Give the position of every leukocyte visible.
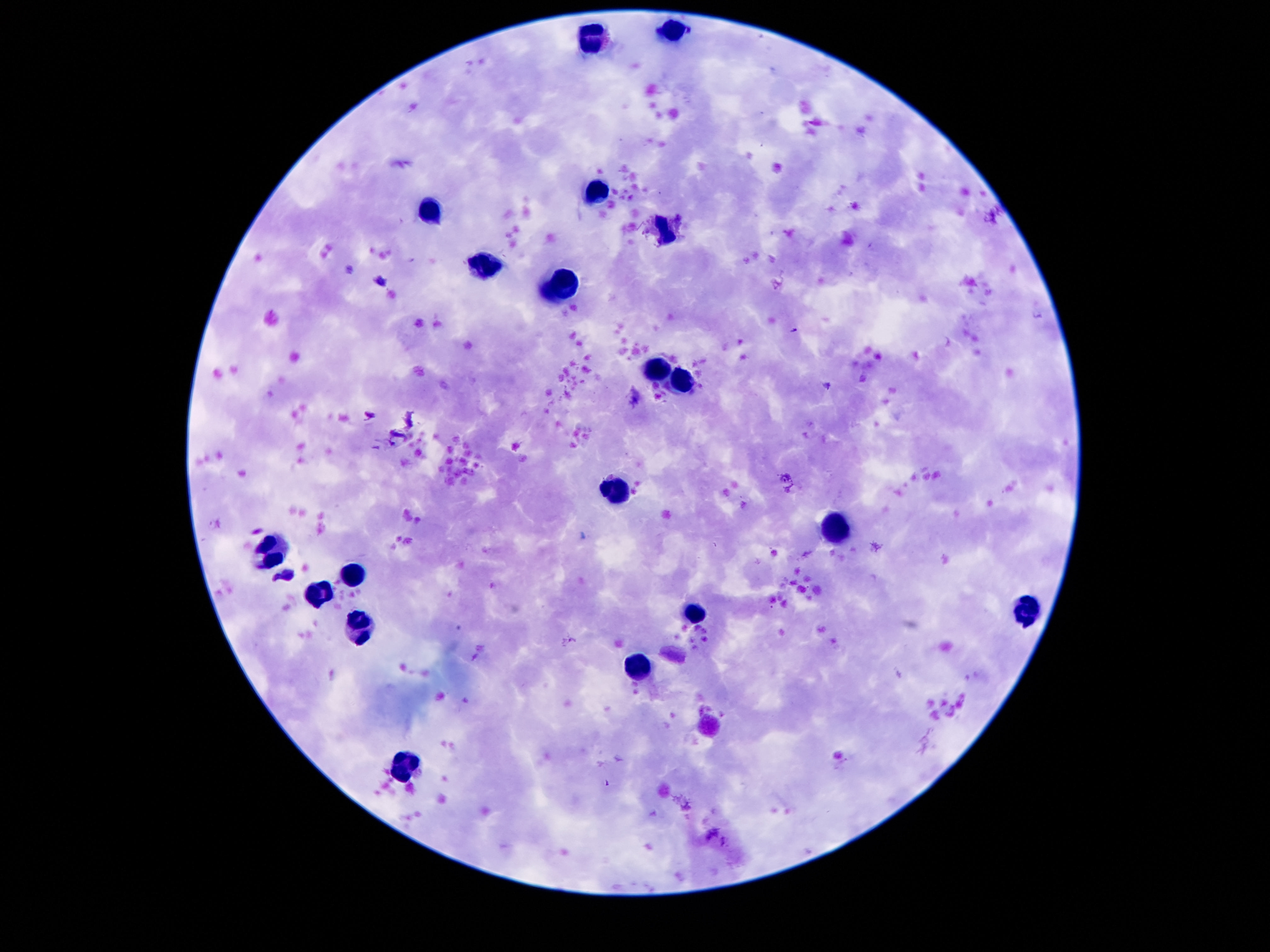

Approximate centers as (x, y) in pixels.
Leukocytes: (673, 33), (593, 38), (593, 189), (433, 210), (667, 232), (491, 265), (560, 283), (659, 369), (683, 380), (616, 490), (839, 529), (273, 554), (351, 574), (320, 593), (693, 611), (1025, 611), (359, 625), (638, 666), (406, 763).

Image is 1270×952 pixels. Single field of view. Smartphone photograph taken through the microscope eyepiece. Giemsa-stained preparation. 100x magnification. Patient malaria status: negative. Thick blood film.